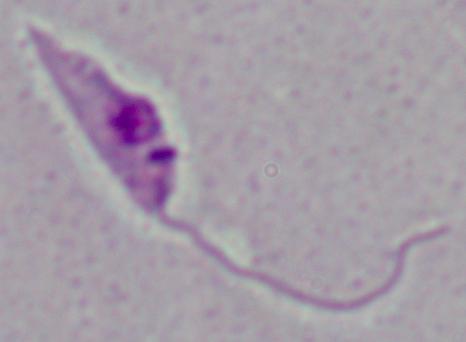
Summary:
  - Modality: micrograph
  - Identification: Leishmania
  - Magnification: 1000x